Describe the morphology of the red blood cells.
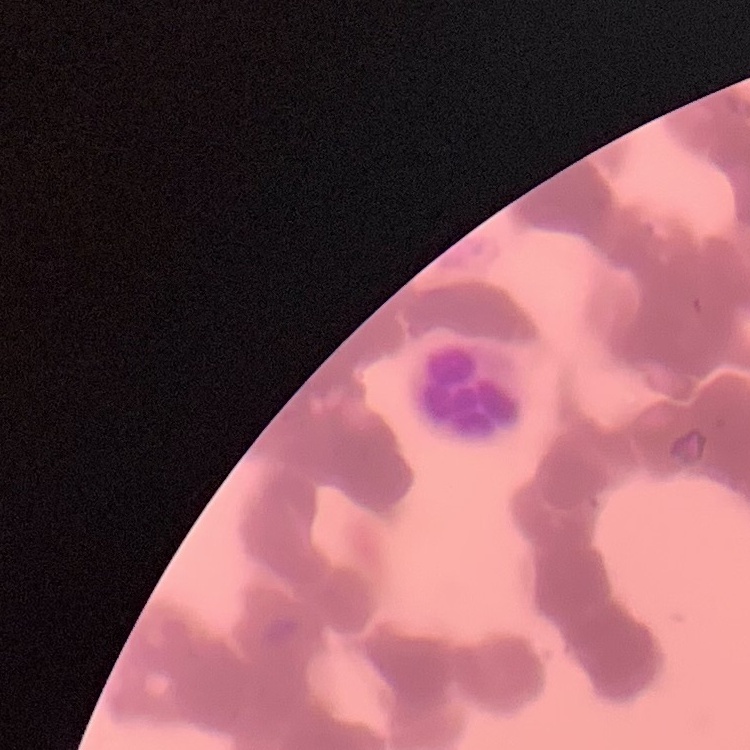

They show rouleaux formation.

Summary:
  - Image type: square crop of a larger photomicrograph
  - Preparation: thin blood film
  - Stain: Field's or Giemsa